State which parasite is depicted.
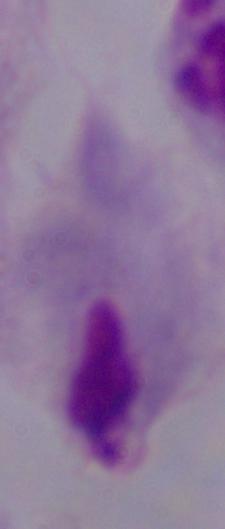
A trichomonad.

1000x magnification. Photomicrograph.